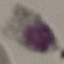

Malaria status: uninfected. Automatically extracted cell patch, resized to 64 × 64 pixels. Acquired by smartphone through the microscope eyepiece. Giemsa-stained preparation. Thin smear of blood.